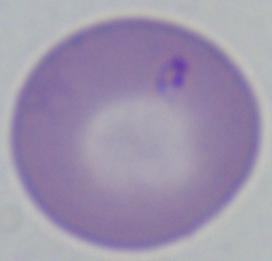

Summary:
  - Magnification: 1000x
  - Modality: photomicrograph
  - Identification: Babesia